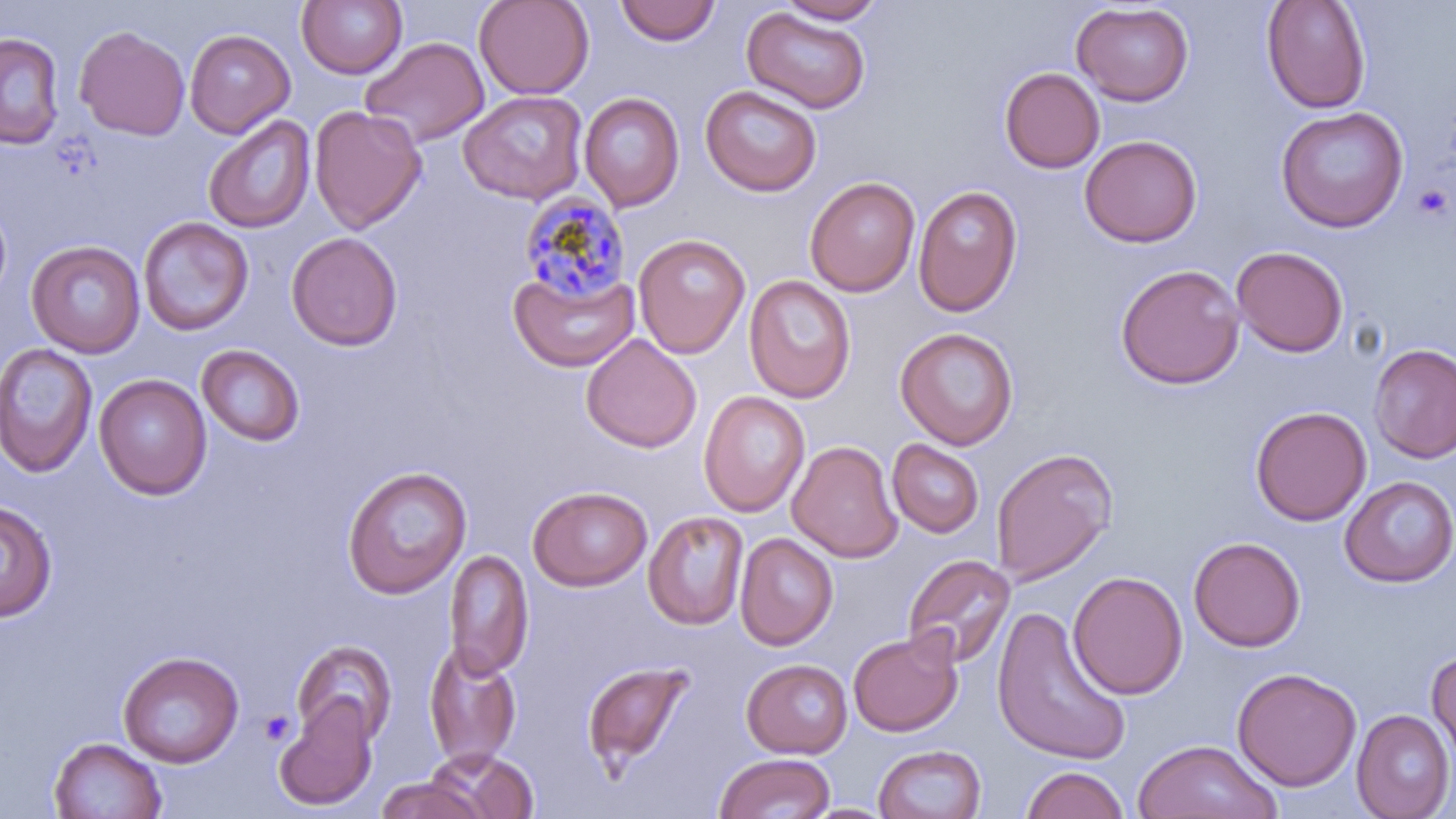 Approximate bounding boxes as [x1, y1, x2, y2] in pixels. Platelet locations: [1411, 182, 1453, 220], [259, 709, 298, 747]. Uninfected red blood cell locations: [473, 0, 594, 100], [614, 0, 722, 46], [1261, 0, 1371, 114], [296, 1, 407, 79], [774, 1, 887, 24], [1071, 2, 1194, 106], [741, 7, 871, 114], [74, 25, 190, 140], [185, 28, 295, 138], [0, 32, 65, 149], [360, 36, 489, 149], [999, 67, 1105, 173], [700, 84, 822, 196], [458, 90, 588, 205], [579, 92, 685, 211], [309, 105, 428, 233], [1275, 106, 1409, 233], [202, 114, 315, 234], [1079, 135, 1202, 248], [804, 177, 920, 297], [913, 185, 1023, 317], [0, 197, 12, 305], [138, 217, 253, 336], [286, 231, 402, 351], [633, 233, 751, 359], [26, 240, 145, 358], [1231, 246, 1348, 357], [1115, 263, 1245, 390], [509, 266, 639, 373], [744, 274, 856, 403], [895, 327, 1018, 449], [581, 334, 701, 453], [0, 342, 99, 478], [196, 344, 306, 447], [1369, 344, 1456, 463], [94, 373, 212, 500], [698, 391, 810, 518], [1250, 405, 1371, 525], [887, 439, 984, 538], [787, 440, 903, 562], [991, 447, 1118, 585], [341, 465, 472, 599], [1340, 476, 1456, 587], [527, 485, 652, 591], [0, 499, 57, 622], [643, 511, 749, 629], [735, 532, 838, 650], [1188, 536, 1305, 652], [442, 548, 533, 679], [902, 553, 1016, 669], [1067, 571, 1187, 700], [992, 605, 1132, 767], [848, 631, 962, 737], [291, 640, 398, 746], [423, 642, 522, 768], [118, 651, 243, 768], [1427, 651, 1456, 774], [741, 658, 853, 758], [581, 659, 695, 776], [1232, 667, 1362, 791], [272, 697, 378, 811], [1352, 709, 1455, 819], [48, 737, 167, 819], [1132, 739, 1281, 819], [873, 743, 986, 819], [422, 748, 539, 819], [712, 753, 835, 818], [1020, 765, 1131, 818], [374, 776, 489, 818], [802, 803, 895, 819]. Plasmodium malariae-infected red blood cell locations: [517, 190, 630, 303]. Slide-level diagnosis: Plasmodium malariae. Optical microscopy. May-Grünwald-Giemsa stain. Single field of view. Image is 1456×819 pixels. Thin blood film. 1000x magnification.